Point out Plasmodium parasites and leukocytes.
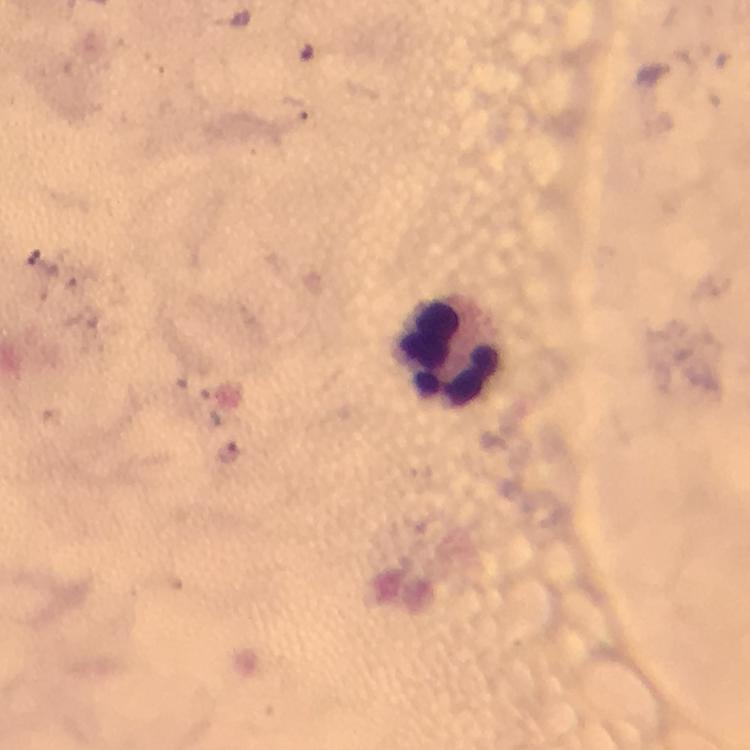
Approximate centers as {x, y} in pixels.
Plasmodium parasites: {231, 452}.
Leukocytes: {451, 349}.

Summary:
  - Preparation: thick smear
  - Capture: smartphone mounted on the microscope
  - Cropped from: a single field of view
  - Immersion oil: applied
  - Image size: 750×750 pixels
  - Magnification: 100x
  - Context: from a malaria diagnostic workup
  - Stain: Giemsa